State the preparation type.
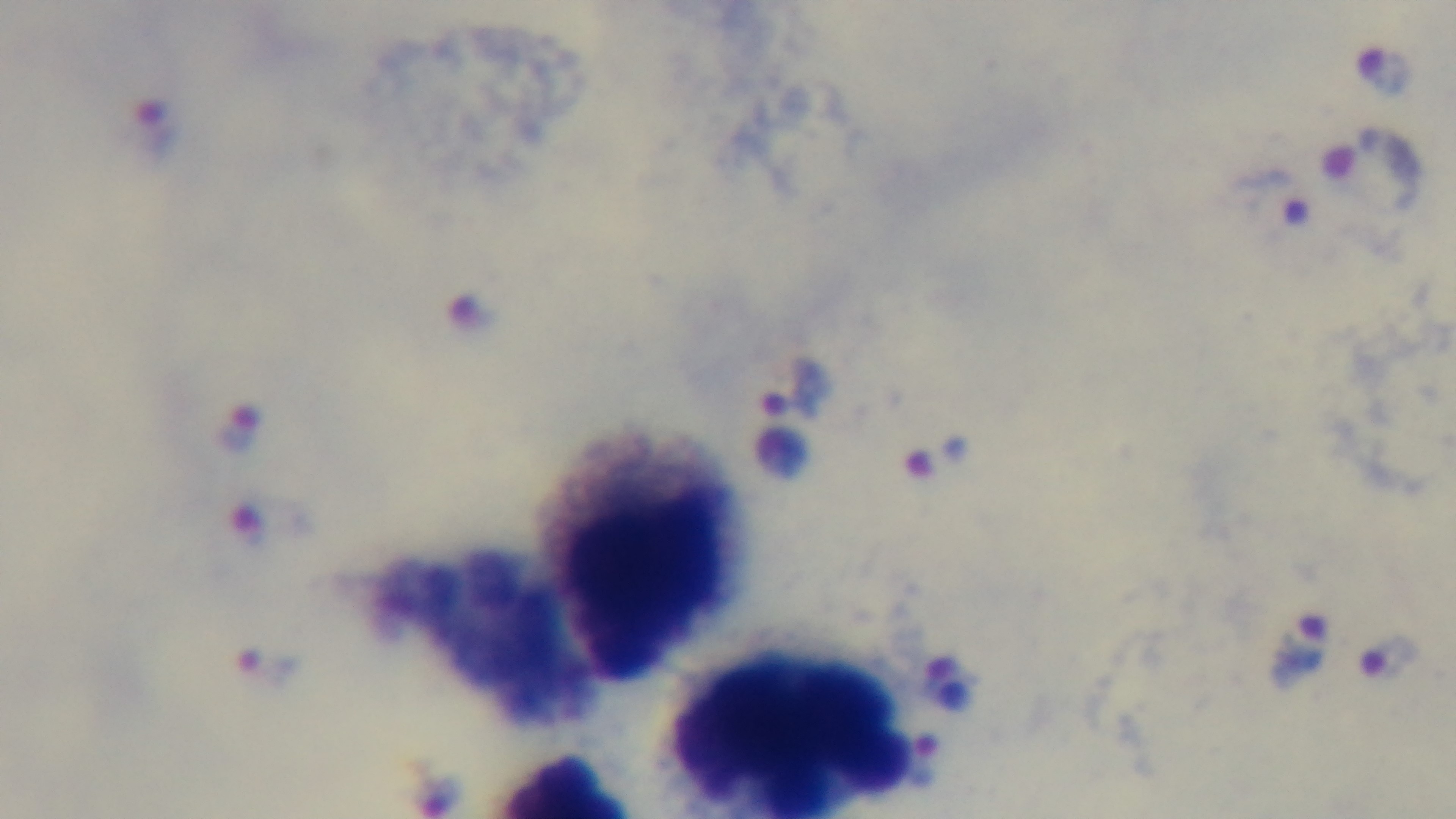

A thick smear.

stain: Giemsa
objective: 100x oil immersion
capture: mounted 4K digital camera
field_of_view: single
modality: light microscopy
malaria_status: infected